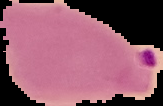 Result: malaria parasites detected. Image is 163×106 pixels. From a thin blood smear. Segmented cell region on a black background.